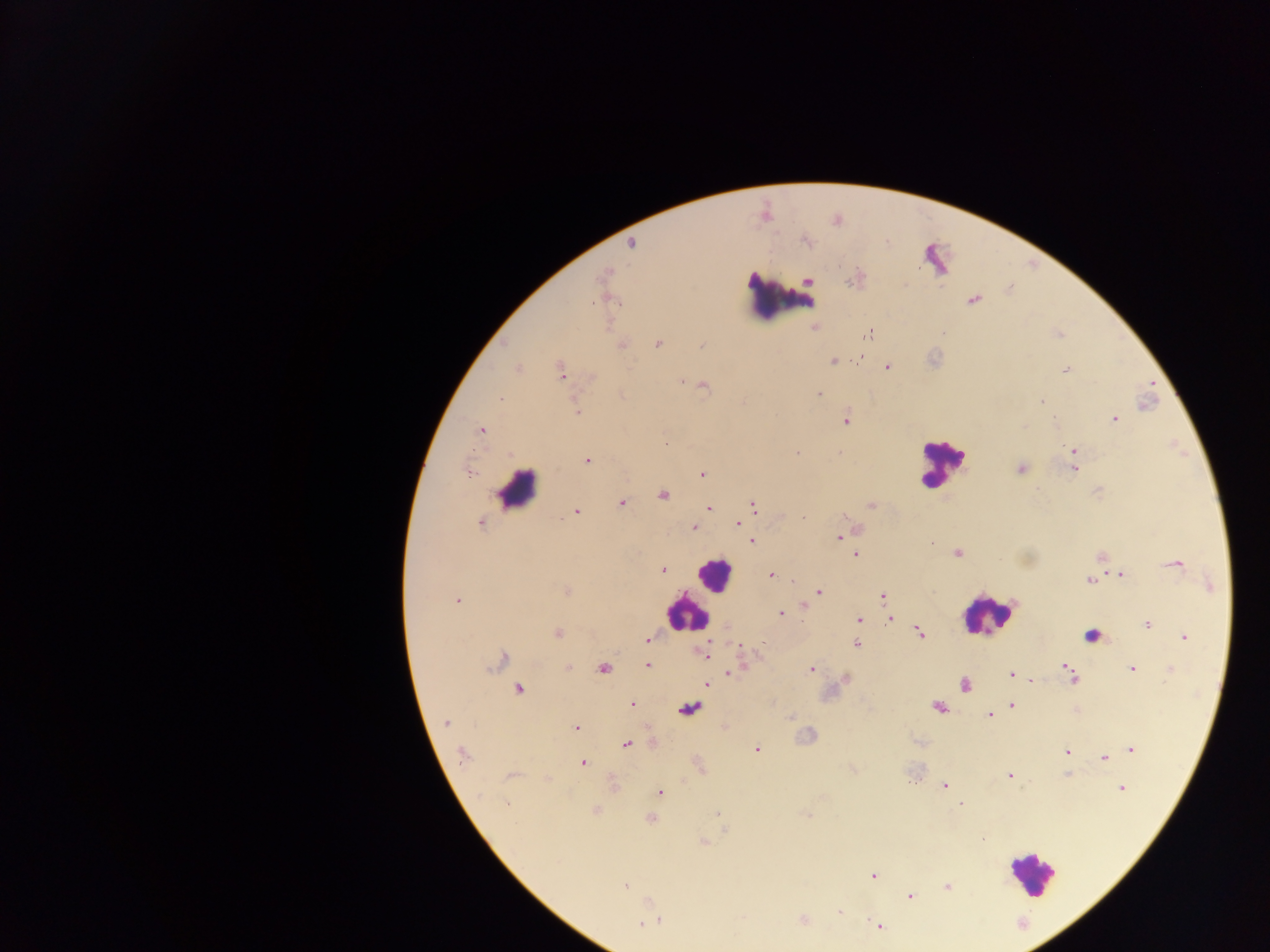
Approximate centers as (x, y) in pixels.
Summary:
  - Malaria parasite locations: (806, 241), (631, 243), (933, 253), (603, 275), (809, 281), (973, 300), (869, 333), (657, 343), (622, 345), (701, 346), (860, 356), (833, 361), (887, 367), (519, 369), (1065, 371), (560, 372), (681, 381), (704, 385), (819, 395), (501, 398), (1041, 402), (577, 412), (1114, 419), (845, 421), (1055, 421), (481, 430), (1074, 450), (796, 453), (587, 461), (1020, 468), (1074, 469), (469, 473), (701, 474), (663, 496), (621, 503), (753, 505), (870, 505), (709, 508), (576, 512), (803, 517), (480, 524), (738, 524), (693, 528), (839, 538), (752, 541), (957, 553), (855, 555), (1176, 564), (663, 569), (771, 575), (1120, 575), (793, 580), (1089, 581), (566, 590), (819, 592), (883, 596), (457, 601), (805, 605), (781, 613), (891, 619), (858, 620), (1147, 624), (920, 633), (557, 634), (1092, 635), (1185, 637), (647, 638), (856, 644), (703, 654), (503, 658), (647, 665), (568, 667), (604, 668), (739, 668), (1067, 668), (1132, 668), (811, 669), (1170, 670), (731, 672), (1011, 674), (1072, 678), (1031, 680), (707, 684), (965, 685), (519, 689), (632, 705), (1011, 705), (937, 707), (690, 708), (989, 715), (445, 723), (576, 727), (626, 745), (757, 749), (1132, 749), (1065, 751), (462, 754), (1104, 758), (583, 763), (512, 776), (1009, 776), (945, 786), (1122, 788), (659, 792), (507, 804), (960, 804), (595, 811), (717, 814), (807, 814), (650, 818), (982, 839), (703, 842), (873, 876), (625, 886), (947, 887), (911, 896), (840, 912), (804, 920), (660, 921), (641, 924), (879, 925)
  - Leukocyte locations: (781, 297), (942, 463), (517, 490), (713, 574), (686, 614), (987, 615), (1031, 873)
  - Image size: 1270×952 pixels
  - Country: Ghana
  - Capture: mobile-phone photograph through a microscope
  - Field of view: single
  - Preparation: thick blood smear